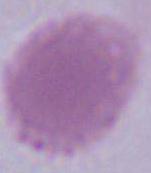
{
  "modality": "photomicrograph",
  "identification": "erythrocyte",
  "magnification": "1000x"
}